Comment on the morphology of the red blood cells.
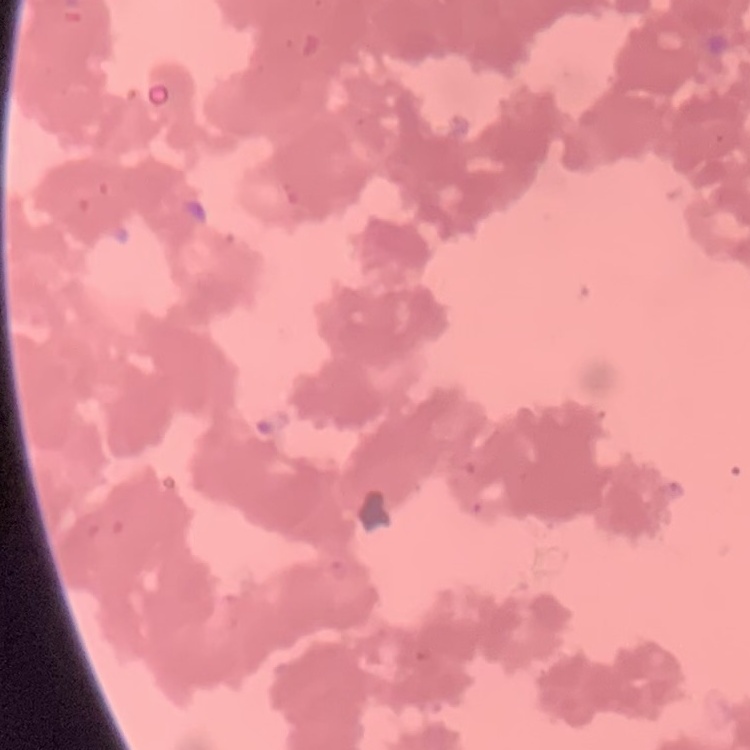
They show rouleaux formation.

image type = one tile cut from a larger photomicrograph
stain = Field's or Giemsa
preparation = thin blood film